Give the preparation type.
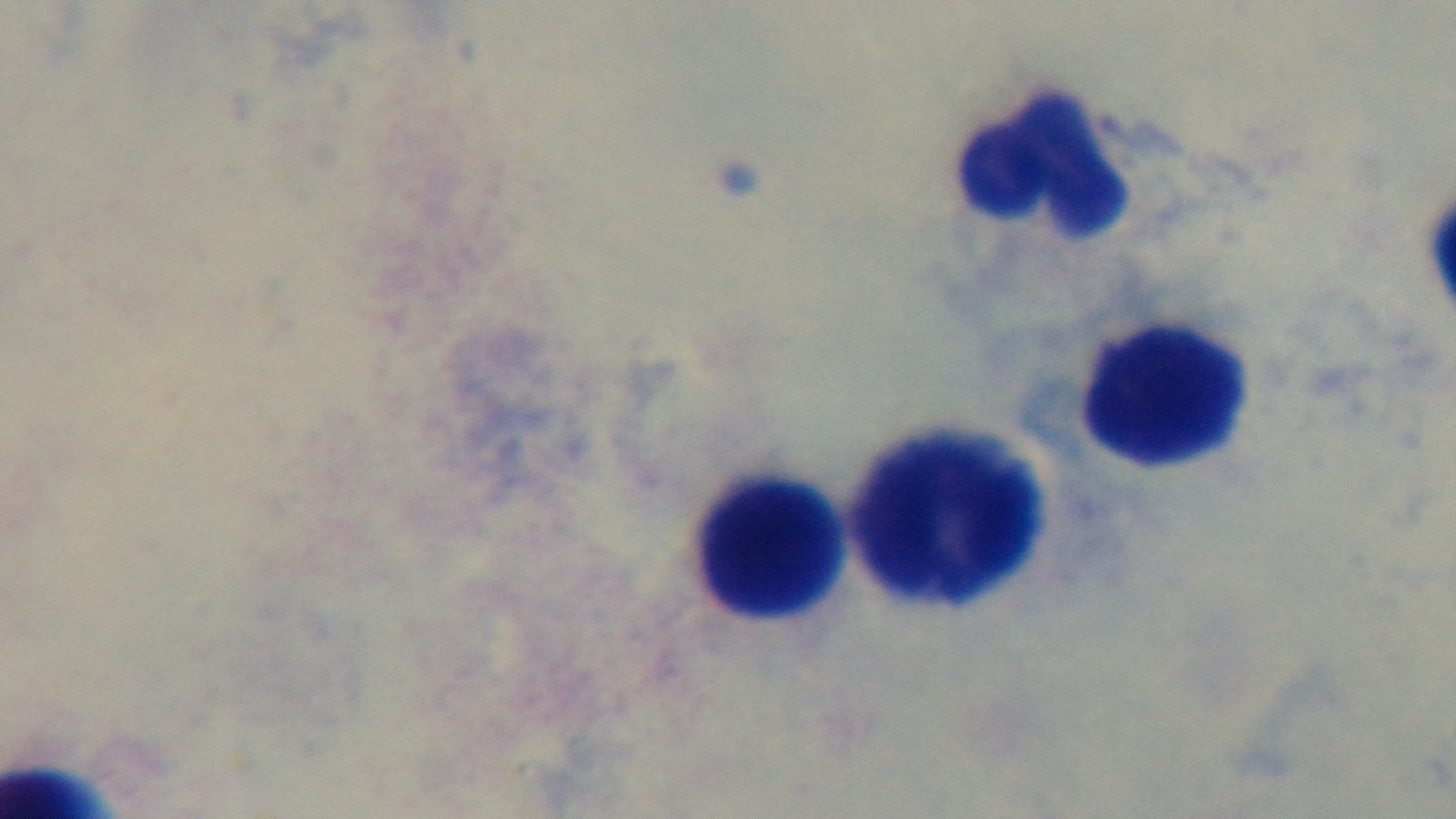

Thick.

Light microscopy. One field from the slide. Giemsa-stained. Malaria status: uninfected. Captured with a mounted 4K digital camera. Oil-immersion objective, 100x.